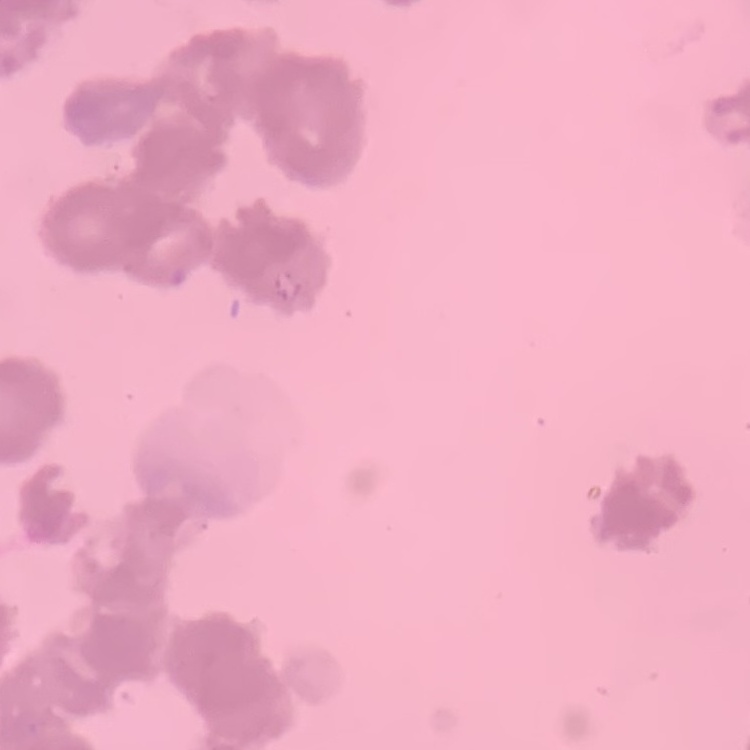 The red blood cells exhibit rouleaux formation. Square crop of a larger photomicrograph. Field's or Giemsa stain. Thin blood film.